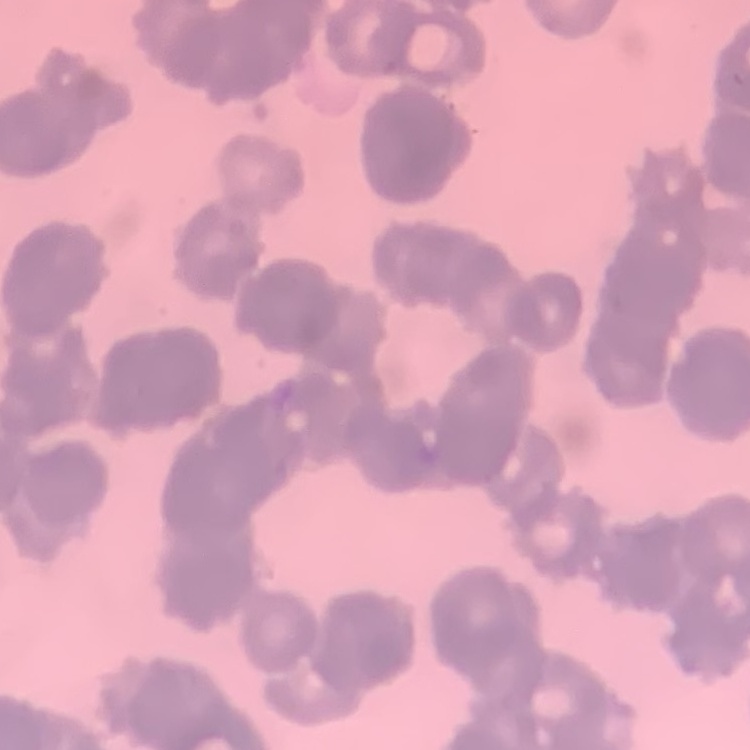

red_blood_cell_morphology: rouleaux formation
image_type: square crop of a larger photomicrograph
stain: Field's or Giemsa
preparation: thin blood film